Describe the morphology of the red blood cells.
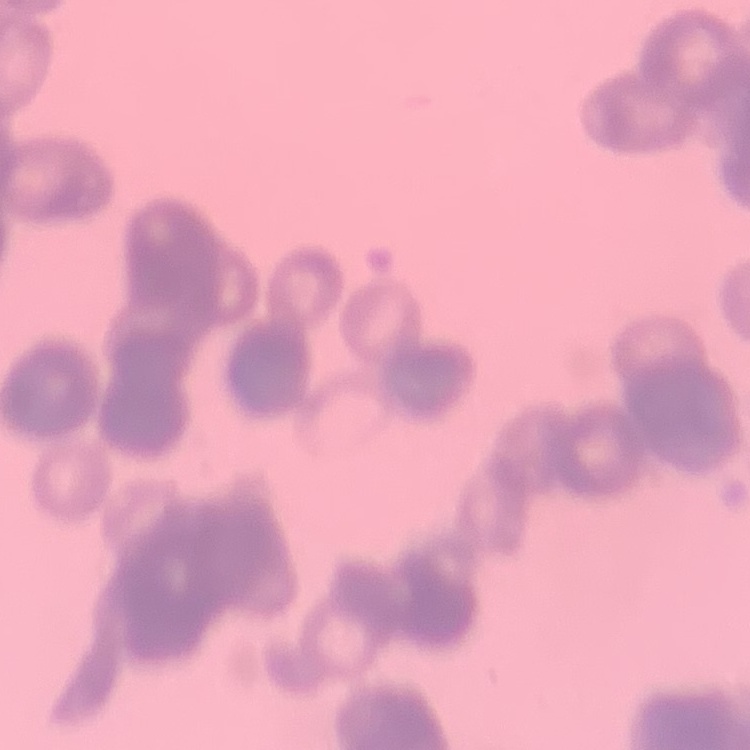

They show rouleaux formation.

Summary:
  - Preparation: thin peripheral smear
  - Stain: Field's or Giemsa
  - Image type: square crop of a larger photomicrograph